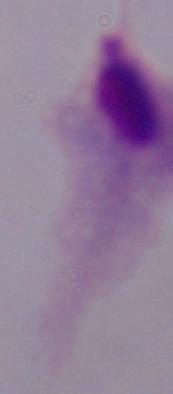

{
  "identification": "trichomonad",
  "modality": "micrograph",
  "magnification": "1000x"
}